Report the malaria status of this cell.
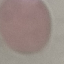
It is uninfected.

Giemsa stain. Thin smear of blood. Photographed with a smartphone camera at the microscope eyepiece. Cell patch, automatically extracted from a larger field of view and resized to 64 × 64 pixels.